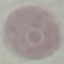

{
  "malaria_status": "uninfected",
  "preparation": "thin smear",
  "stain": "Giemsa",
  "image_type": "automatically extracted cell patch, resized to 64 × 64 pixels",
  "capture": "smartphone camera at the microscope eyepiece"
}